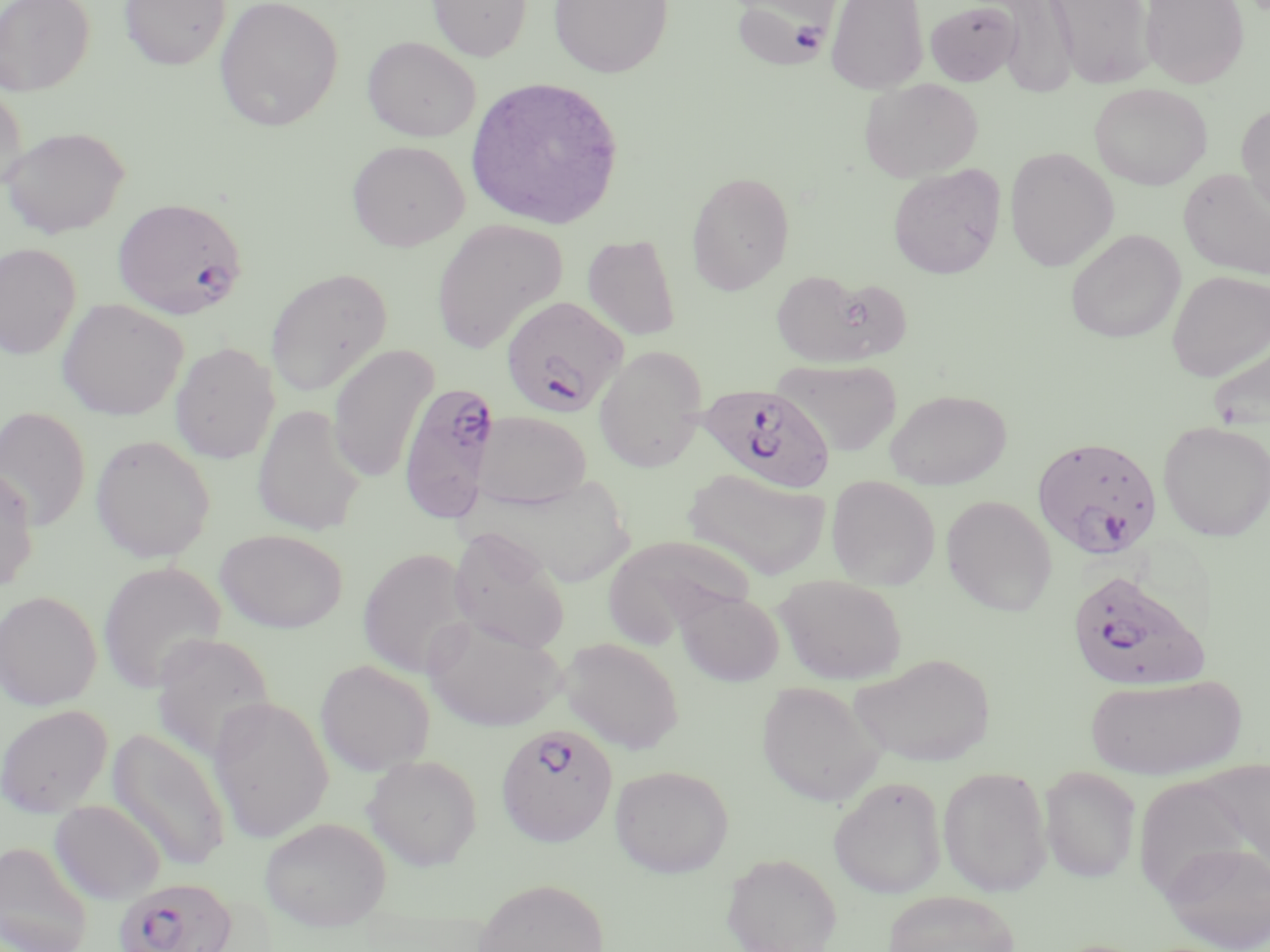
{
  "plasmodium_falciparum_infected_red_blood_cell_locations": "approximate bounding boxes as (x1, y1, x2, y2) in pixels: (731, 0, 836, 71), (113, 197, 248, 320), (501, 295, 628, 417), (397, 381, 500, 523), (699, 383, 836, 493), (1035, 435, 1165, 558), (1067, 570, 1208, 692), (495, 723, 617, 848), (113, 876, 238, 952)",
  "slide_level_diagnosis": "Plasmodium falciparum",
  "preparation": "thin blood smear",
  "magnification": "1000x",
  "field_of_view": "single",
  "modality": "light microscopy",
  "stain": "May-Grünwald-Giemsa",
  "image_size": "1270×952 pixels",
  "uninfected_red_blood_cell_locations": "approximate bounding boxes as (x1, y1, x2, y2) in pixels: (0, 0, 94, 95), (119, 0, 230, 69), (215, 0, 343, 131), (427, 0, 532, 61), (548, 0, 673, 78), (826, 0, 929, 94), (1048, 0, 1155, 88), (1140, 0, 1249, 88), (924, 1, 1022, 86), (996, 1, 1079, 98), (363, 36, 481, 142), (464, 76, 624, 230), (860, 78, 984, 181), (0, 81, 27, 193), (1088, 83, 1212, 190), (1236, 102, 1270, 218), (1, 126, 129, 238), (347, 140, 469, 251), (1004, 147, 1118, 271), (888, 164, 1006, 279), (1179, 167, 1270, 280), (686, 171, 795, 295), (431, 220, 568, 354), (1065, 229, 1185, 343), (582, 234, 682, 341), (0, 242, 82, 360), (264, 268, 393, 397), (770, 268, 900, 367), (1166, 270, 1269, 382), (57, 298, 188, 420), (1207, 336, 1270, 434), (169, 341, 280, 463), (327, 344, 438, 484), (593, 346, 708, 473), (776, 359, 902, 457), (885, 389, 1012, 490), (251, 404, 366, 537), (0, 407, 90, 531), (474, 410, 591, 510), (1157, 420, 1270, 541), (90, 434, 215, 563), (0, 466, 38, 593), (682, 468, 833, 582), (484, 474, 637, 589), (826, 476, 940, 590), (941, 495, 1057, 616), (448, 527, 570, 653), (215, 529, 348, 634), (602, 535, 755, 646), (357, 547, 476, 679), (97, 560, 227, 695), (775, 574, 907, 685), (0, 590, 102, 710), (675, 590, 784, 686), (422, 614, 566, 732), (151, 633, 276, 763), (559, 637, 684, 754), (850, 653, 997, 767), (315, 659, 436, 776), (1085, 673, 1247, 779), (756, 681, 886, 806), (208, 696, 334, 844), (0, 704, 113, 817), (107, 728, 232, 873), (363, 753, 482, 870), (610, 764, 734, 878), (938, 766, 1052, 897), (1039, 766, 1142, 883), (828, 775, 946, 899), (50, 800, 166, 904), (259, 816, 392, 932), (0, 840, 93, 952), (1161, 842, 1270, 951), (720, 852, 842, 952), (470, 877, 610, 952), (882, 890, 1020, 952)"
}